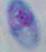
Summary:
  - Modality: micrograph
  - Identification: Toxoplasma gondii
  - Magnification: 1000x